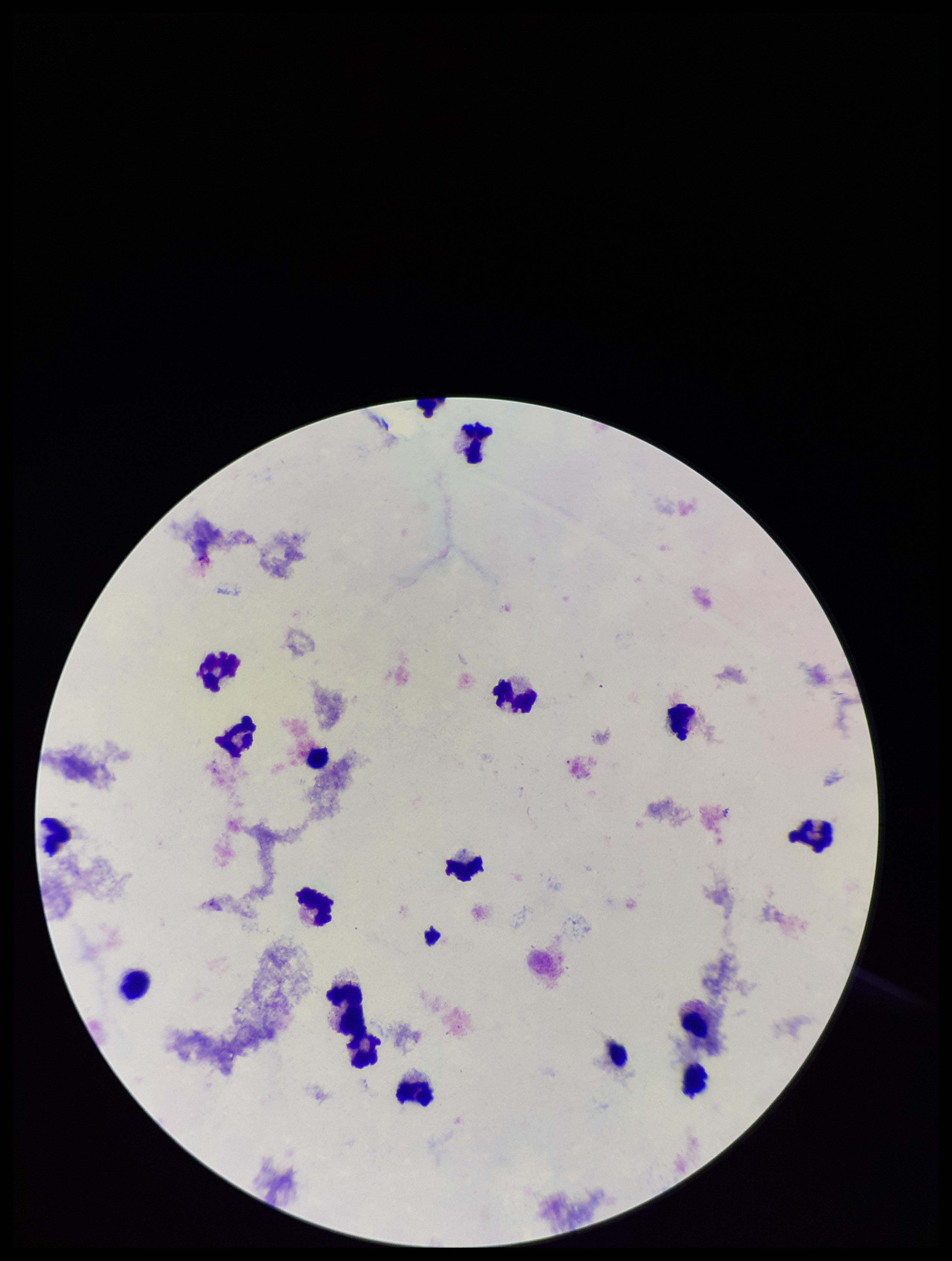 Patient malaria status: negative. Leukocyte count: 16. Single field of view. Plasmodium parasites: none detected. Giemsa stain. Parasite count: 0. Preparation: thick smear. Smartphone photograph taken through the eyepiece of a microscope. Image is 952×1261 pixels.